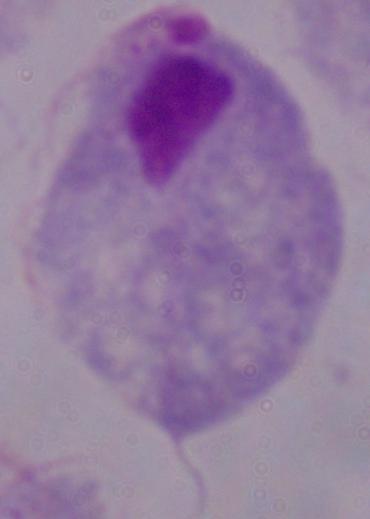

{
  "modality": "photomicrograph",
  "identification": "trichomonad",
  "magnification": "1000x"
}